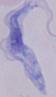
Summary:
  - Identification: trypanosome
  - Magnification: 1000x
  - Modality: micrograph